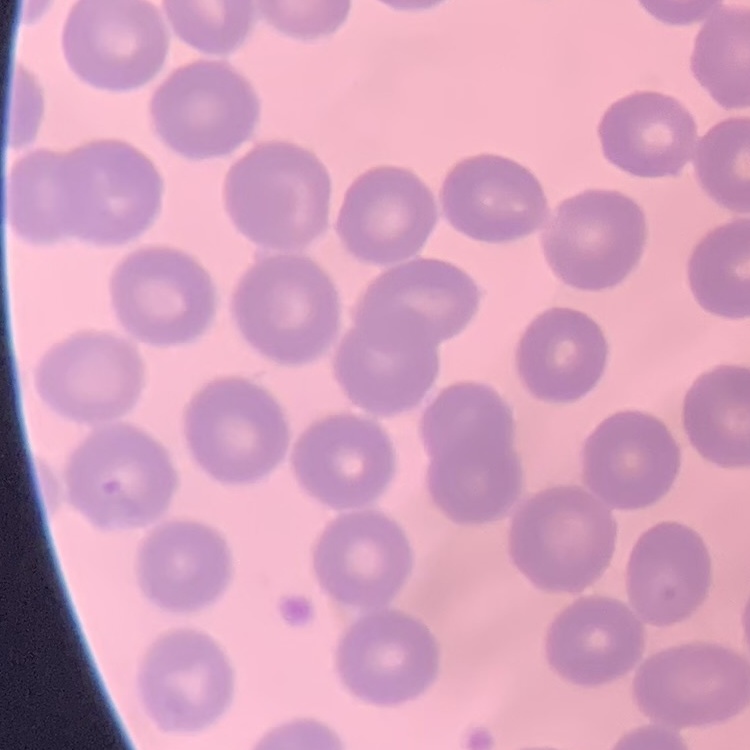

Summary:
  - Erythrocyte morphology: no rouleaux formation
  - Stain: Field's or Giemsa
  - Preparation: thin blood film
  - Image type: square crop of a larger photomicrograph